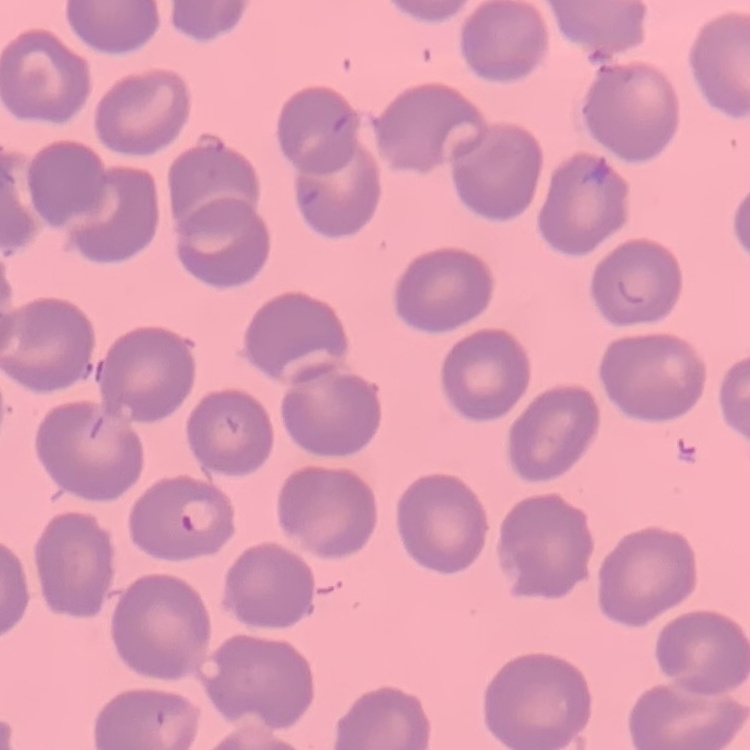
Summary:
  - Red blood cell morphology: no rouleaux formation
  - Preparation: thin blood film
  - Stain: Field's or Giemsa
  - Image type: one tile cut from a larger photomicrograph